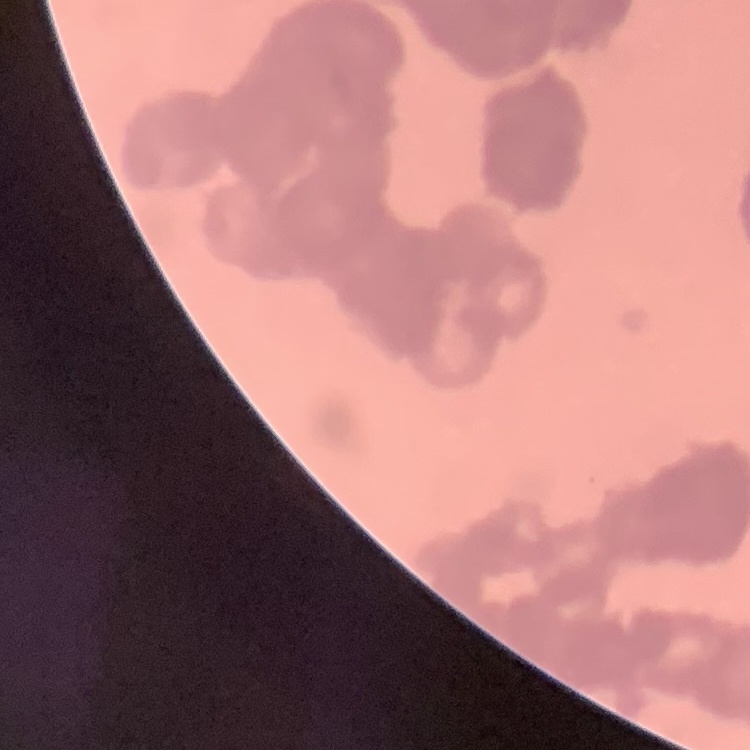

red blood cell morphology = rouleaux formation
image type = square crop of a larger photomicrograph
stain = Field's or Giemsa
preparation = thin blood smear